Give the position of every Plasmodium parasite.
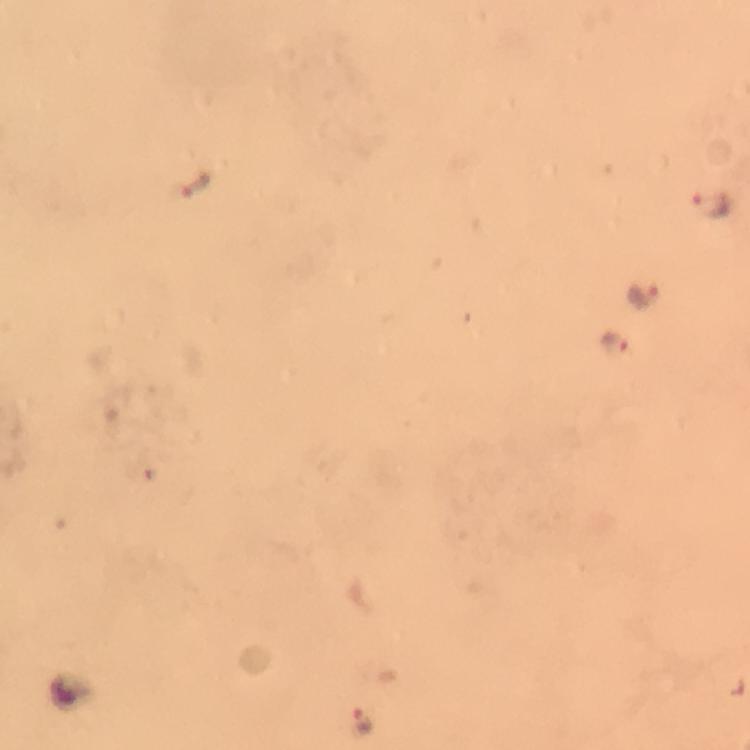
Approximate object centers, in pixels from the top-left corner.
Plasmodium parasites: (x=194, y=185), (x=715, y=208), (x=642, y=296), (x=615, y=342), (x=362, y=719).

image size = 750×750 pixels
capture = smartphone photograph through a microscope
context = from a malaria diagnostic workup
stain = Giemsa
preparation = thick smear
cropped from = a single field of view
immersion oil = applied
magnification = 100x